Name the parasite shown.
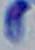
This is Toxoplasma gondii.

{
  "magnification": "1000x",
  "modality": "micrograph"
}